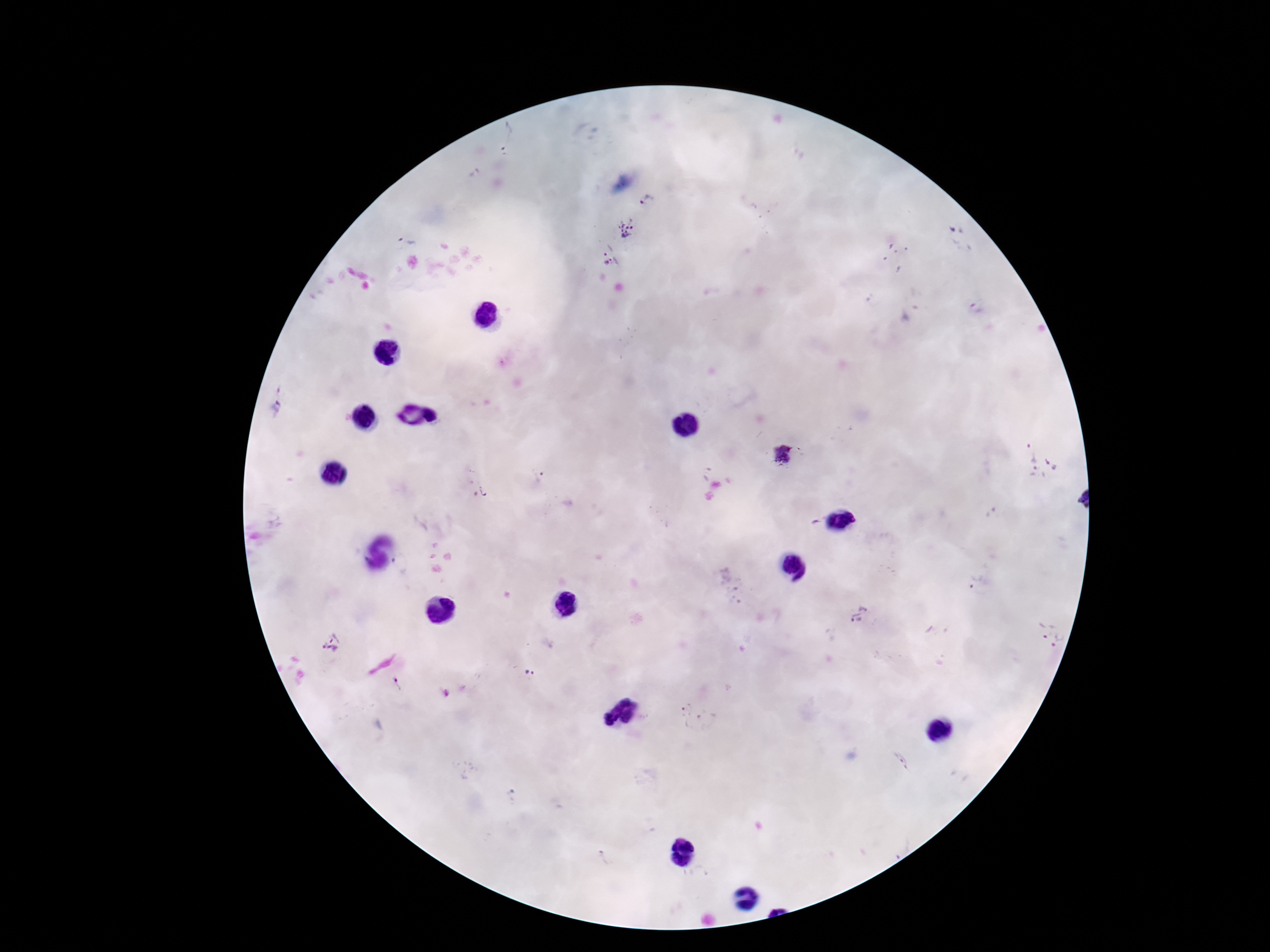
Plasmodium parasite locations = approximate centers as (x, y) in pixels: (505, 138), (647, 200), (626, 227), (957, 229), (408, 241), (606, 250), (615, 261), (976, 309), (274, 409), (1029, 452), (781, 453), (1052, 462), (1036, 473), (539, 476), (485, 489), (975, 581), (731, 586), (860, 613), (1044, 630), (330, 641), (1058, 642), (530, 673), (397, 686), (691, 713), (899, 760), (602, 858)
magnification = 100x
image size = 1270×952 pixels
stain = Giemsa
capture = smartphone camera through the microscope eyepiece
preparation = thick blood film
field of view = one from this slide
patient malaria status = infected